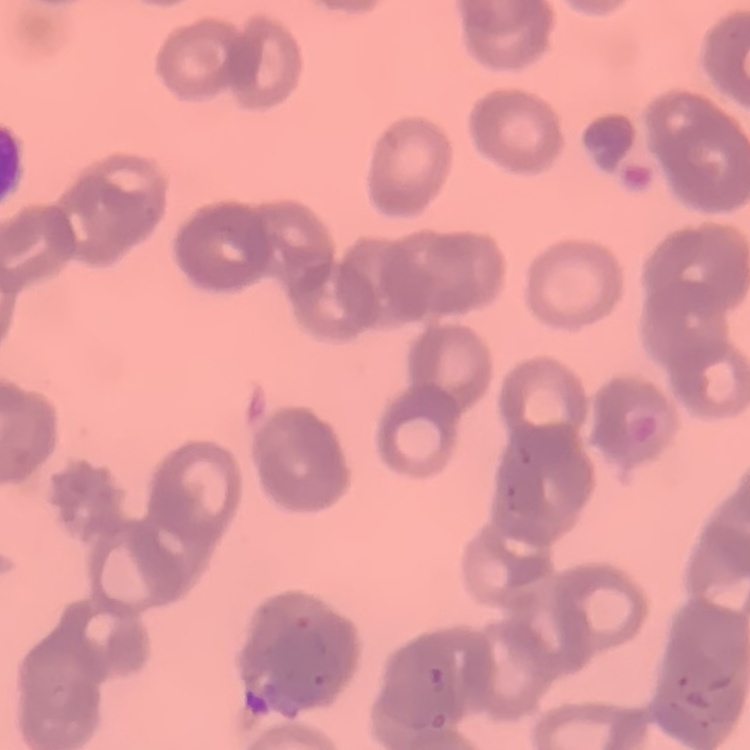

Summary:
  - Red blood cell morphology: rouleaux formation
  - Stain: Field's or Giemsa
  - Image type: square crop of a larger photomicrograph
  - Preparation: thin blood film